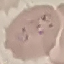

{
  "result": "malaria parasites detected",
  "preparation": "thin blood film",
  "capture": "smartphone camera at the microscope eyepiece",
  "stain": "Giemsa",
  "image_type": "automatically extracted cell patch, resized to 64 × 64 pixels"
}